Outline each blood parasite and name the species.
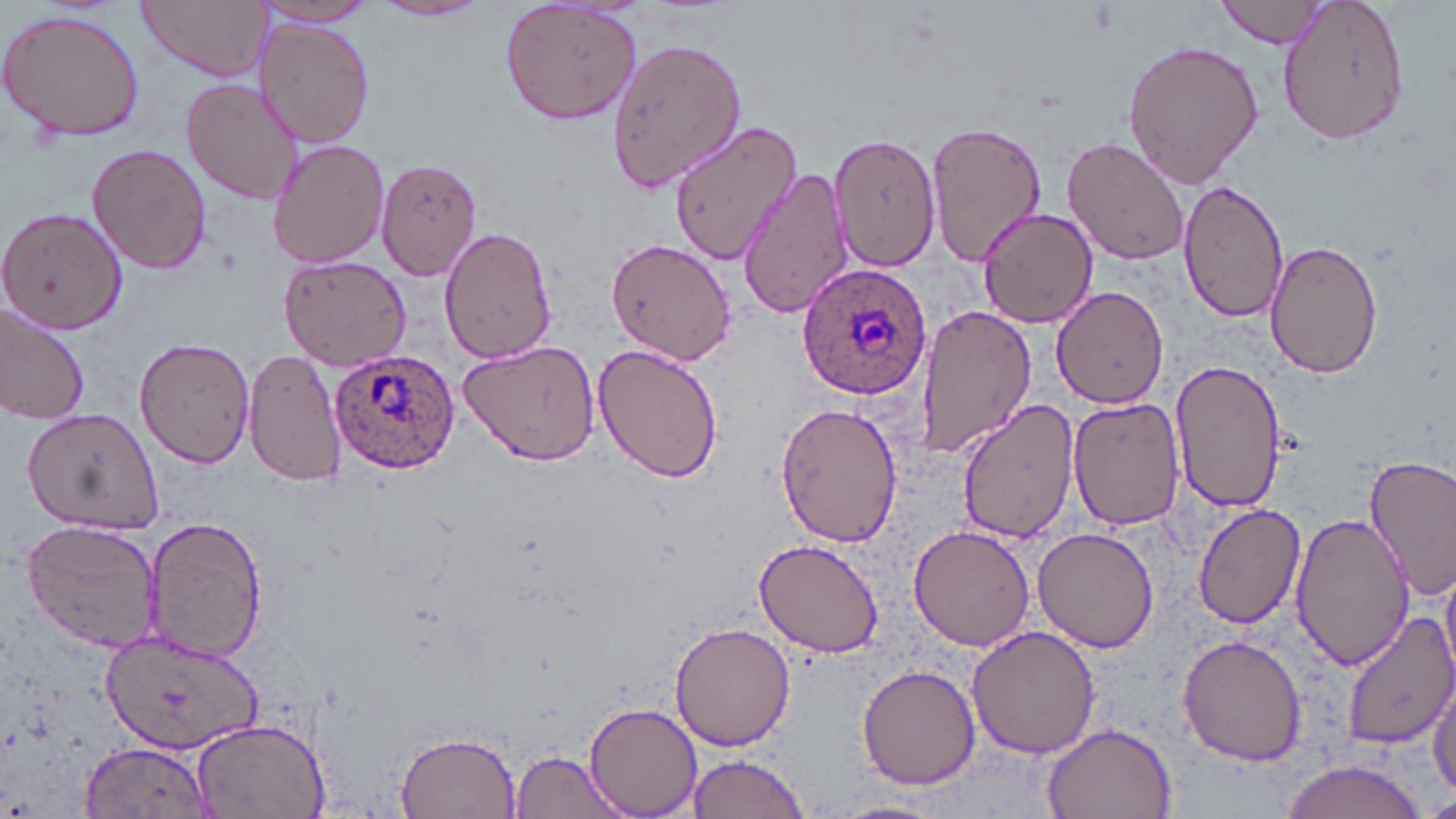
Approximate bounding boxes as (x1,y1)-(x2,y2) corner pairs in pixels.
Plasmodium ovale-infected red blood cells: (797,261)-(932,399), (330,354)-(459,474).
No Plasmodium falciparum, Plasmodium malariae, Plasmodium vivax, Babesia divergens, or Trypanosoma brucei observed.

Summary:
  - Uninfected red blood cell locations: (139,0)-(272,82), (373,0)-(489,22), (499,0)-(646,125), (1218,0)-(1331,49), (1276,0)-(1410,145), (253,2)-(384,28), (0,9)-(146,141), (255,19)-(374,147), (606,37)-(746,192), (1121,38)-(1264,189), (180,78)-(303,206), (924,118)-(1049,264), (669,122)-(804,268), (831,135)-(941,271), (1064,136)-(1190,266), (267,137)-(389,270), (86,143)-(213,275), (376,157)-(483,280), (736,167)-(855,317), (1176,178)-(1289,321), (0,207)-(127,333), (976,207)-(1100,329), (438,225)-(556,365), (1266,237)-(1381,379), (607,239)-(736,365), (279,252)-(414,368), (1051,286)-(1169,408), (912,304)-(1037,459), (0,306)-(91,426), (134,337)-(257,467), (459,340)-(603,466), (592,342)-(724,485), (244,346)-(347,490), (1171,359)-(1287,512), (1068,396)-(1186,532), (957,398)-(1079,546), (773,400)-(904,548), (24,408)-(161,533), (1363,456)-(1456,597), (1192,501)-(1305,629), (1290,511)-(1416,670), (143,517)-(266,664), (20,519)-(162,653), (907,522)-(1038,651), (1033,527)-(1158,653), (753,538)-(885,658), (1442,563)-(1456,672), (1338,610)-(1456,749), (670,622)-(796,752), (965,625)-(1099,760), (102,626)-(264,757), (1177,633)-(1309,765), (856,664)-(980,790), (1429,681)-(1455,800), (583,701)-(703,816), (188,718)-(330,818), (1041,722)-(1178,819), (394,730)-(519,816), (80,741)-(216,818), (508,751)-(628,817), (682,754)-(812,819), (1276,762)-(1436,819), (1425,790)-(1456,819), (828,798)-(951,819)
  - Slide-level diagnosis: Plasmodium ovale
  - Image size: 1456×819 pixels
  - Preparation: thin blood smear
  - Modality: optical microscopy
  - Magnification: 1000x
  - Field of view: single
  - Stain: May-Grünwald-Giemsa